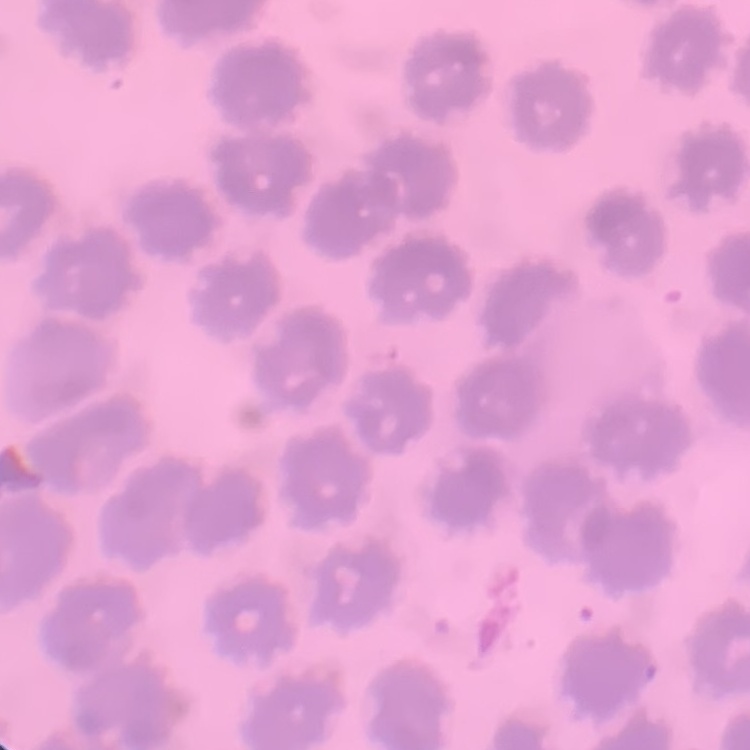

{
  "red_blood_cell_morphology": "no rouleaux formation",
  "image_type": "square crop of a larger photomicrograph",
  "stain": "Field's or Giemsa",
  "preparation": "thin blood film"
}